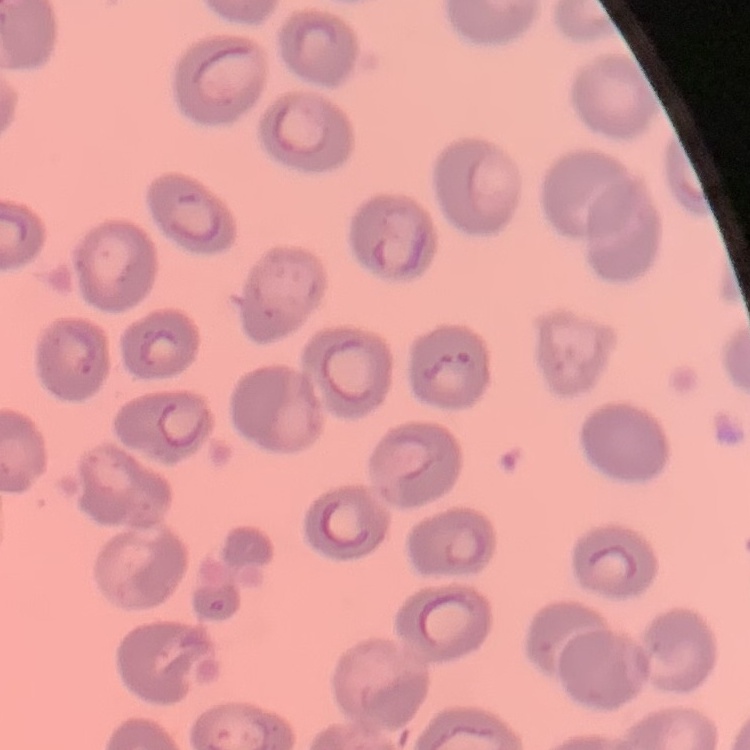
The erythrocytes show no rouleaux formation. Thin blood smear. Stained with either Field's or Giemsa. Square crop of a larger photomicrograph.